Assess the morphology of the red blood cells.
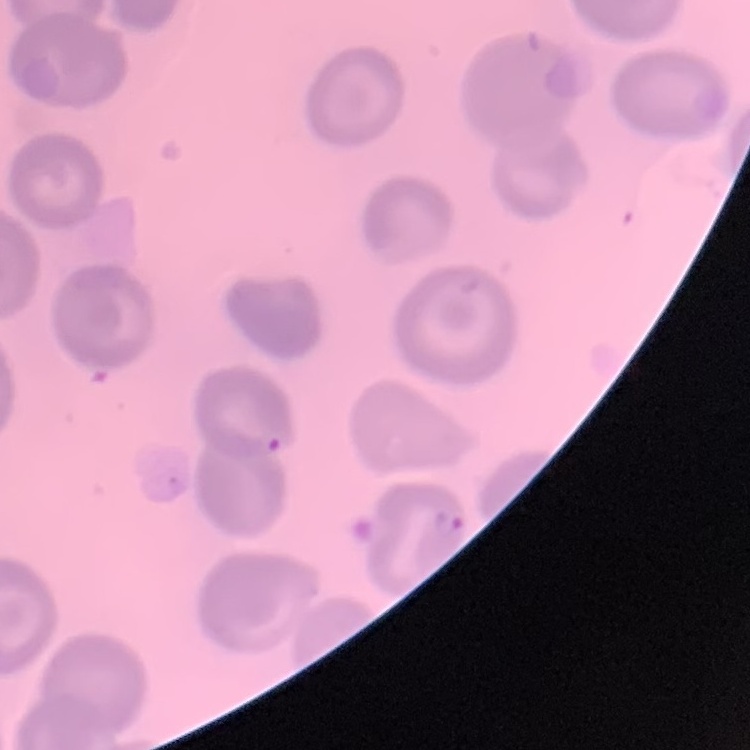
They show no rouleaux formation.

Thin blood film. Square crop of a larger photomicrograph. Stained with either Field's or Giemsa.